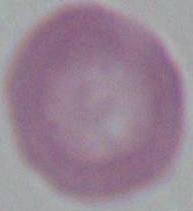

Captured at 1000x magnification. Photomicrograph. A red blood cell is shown.